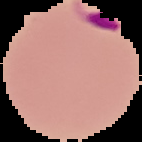

image size = 142×142 pixels
malaria status = parasitized
preparation = thin blood film
image type = segmented cell region on a black background